Describe the morphology of the red blood cells.
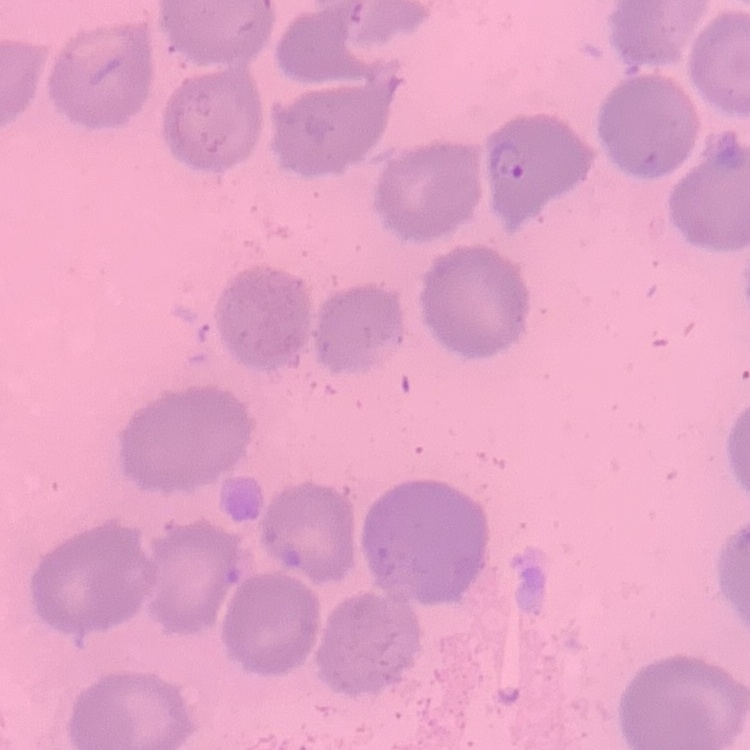
No rouleaux formation.

Stained with either Field's or Giemsa. One tile cut from a larger photomicrograph. Thin blood film.